Report the malaria status of this cell.
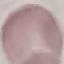

It is uninfected.

preparation = thin blood film
image type = cell patch, automatically extracted from a larger field of view and resized to 64 × 64 pixels
stain = Giemsa
capture = smartphone through the microscope eyepiece